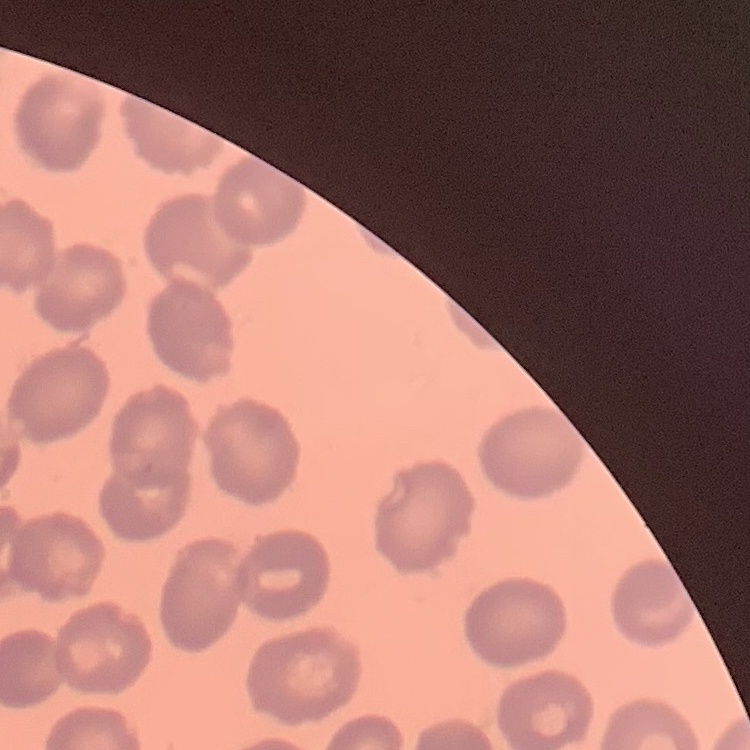

The erythrocytes exhibit no rouleaux formation. Thin blood smear. One tile cut from a larger photomicrograph. Field's or Giemsa stain.